Classify this cell by malaria status.
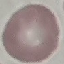

It is uninfected.

Giemsa-stained preparation. Thin blood smear. Cell patch, automatically extracted from a larger field of view and resized to 64 × 64 pixels. Photographed with a smartphone camera at the microscope eyepiece.